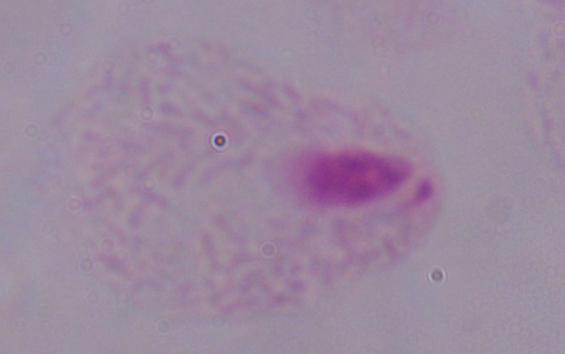
{
  "identification": "trichomonad",
  "modality": "micrograph",
  "magnification": "1000x"
}